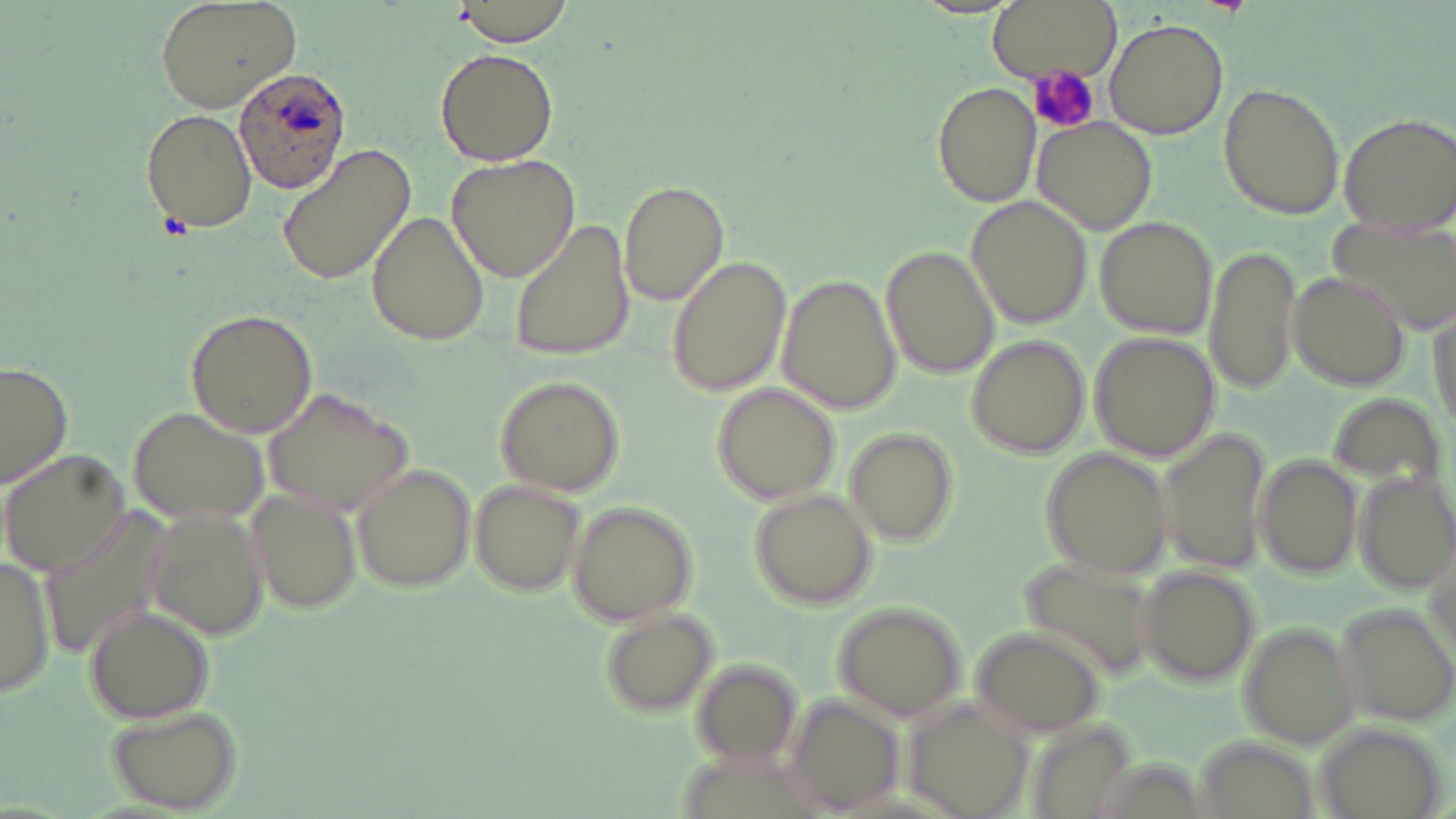
slide-level diagnosis = Plasmodium ovale
modality = optical microscopy
Plasmodium ovale-infected red blood cell locations = approximate bounding boxes as (x1,y1)-(x2,y2) corner pairs in pixels: (232,66)-(351,194)
preparation = thin blood smear
field of view = single
stain = May-Grünwald-Giemsa
image size = 1456×819 pixels
magnification = 1000x
uninfected red blood cell locations = approximate bounding boxes as (x1,y1)-(x2,y2) corner pairs in pixels: (154,0)-(301,113), (987,0)-(1120,79), (451,1)-(575,47), (1104,19)-(1227,140), (435,48)-(559,167), (933,81)-(1041,209), (1216,82)-(1346,220), (140,106)-(258,235), (1334,112)-(1456,230), (1035,118)-(1158,235), (275,144)-(417,289), (446,155)-(580,283), (618,183)-(729,311), (966,195)-(1095,329), (367,210)-(490,348), (1322,210)-(1456,332), (1095,216)-(1216,337), (509,218)-(637,362), (1205,242)-(1301,396), (881,246)-(999,379), (665,254)-(790,400), (1286,269)-(1412,394), (781,273)-(900,415), (183,308)-(320,438), (1089,332)-(1217,463), (966,335)-(1092,458), (0,361)-(73,489), (495,374)-(625,497), (711,382)-(843,505), (264,386)-(414,516), (1325,389)-(1447,489), (126,406)-(263,528), (1160,426)-(1273,579), (844,428)-(958,547), (1038,445)-(1174,582), (2,448)-(133,576), (1250,452)-(1364,580), (351,464)-(476,594), (1355,468)-(1456,594), (469,478)-(588,598), (244,484)-(363,614), (747,487)-(876,608), (43,500)-(180,661), (567,503)-(698,626), (140,504)-(267,643), (0,552)-(55,700), (1015,554)-(1165,687), (1132,564)-(1264,686), (1335,601)-(1456,728), (832,602)-(968,723), (82,605)-(214,723), (597,608)-(720,719), (1237,622)-(1358,751), (970,626)-(1106,738), (689,658)-(801,769), (785,695)-(905,816), (103,704)-(245,812), (907,704)-(1037,819), (1027,716)-(1144,819)
platelet locations = approximate bounding boxes as (x1,y1)-(x2,y2) corner pairs in pixels: (1028,65)-(1101,134)